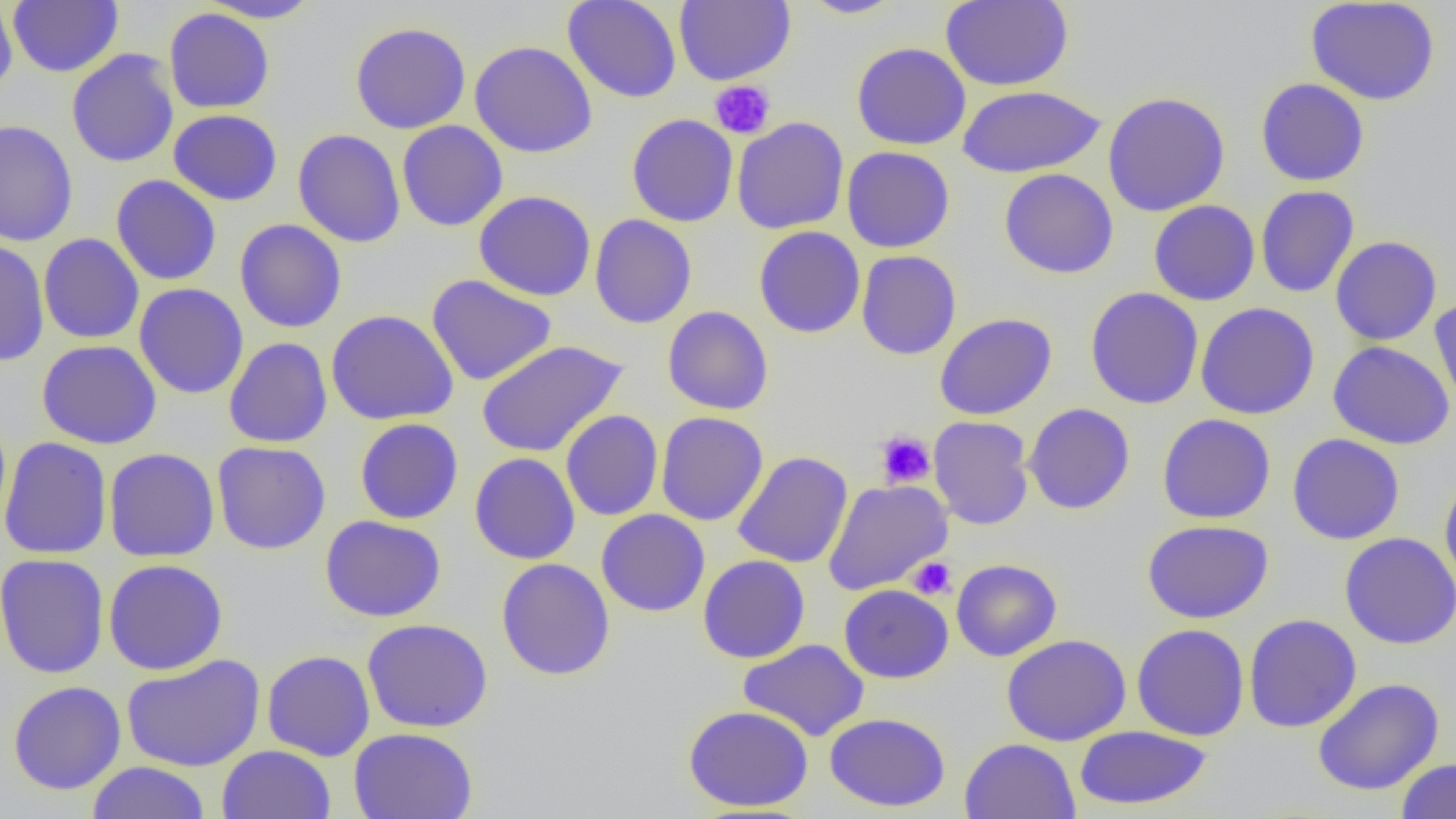 Approximate bounding boxes as (x1,y1)-(x2,y2) corner pairs in pixels. Platelet locations: (709,80)-(775,139), (875,430)-(935,489), (908,557)-(956,599). Uninfected red blood cell locations: (0,0)-(18,97), (197,0)-(325,23), (562,0)-(682,103), (674,0)-(795,86), (797,0)-(908,19), (940,0)-(1073,91), (8,1)-(123,77), (1304,1)-(1440,106), (164,8)-(274,113), (350,21)-(472,134), (470,40)-(598,158), (851,42)-(971,150), (66,49)-(179,168), (1255,77)-(1369,186), (958,85)-(1106,178), (1102,91)-(1230,216), (168,109)-(282,206), (626,113)-(739,226), (732,116)-(849,234), (0,120)-(79,247), (397,120)-(508,231), (293,128)-(406,248), (841,146)-(956,253), (999,168)-(1118,279), (111,174)-(222,285), (1255,185)-(1360,298), (473,190)-(596,301), (1148,200)-(1260,306), (589,214)-(697,329), (234,219)-(347,333), (754,226)-(865,338), (38,233)-(144,344), (1331,236)-(1442,345), (0,237)-(49,366), (856,250)-(962,360), (426,274)-(557,386), (134,283)-(249,399), (1085,287)-(1203,409), (1429,298)-(1456,416), (1195,302)-(1320,420), (662,306)-(774,415), (326,308)-(459,426), (934,313)-(1057,420), (224,337)-(333,448), (36,339)-(162,449), (476,339)-(629,458), (1327,340)-(1454,450), (1023,403)-(1135,515), (561,410)-(663,521), (655,411)-(769,526), (1157,413)-(1276,524), (929,416)-(1035,530), (354,418)-(464,524), (1287,433)-(1405,545), (0,437)-(112,559), (212,441)-(331,554), (103,447)-(220,562), (733,451)-(853,568), (469,452)-(580,565), (1439,472)-(1456,595), (823,479)-(952,595), (596,509)-(710,616), (320,514)-(446,622), (1142,520)-(1274,623), (1339,532)-(1456,650), (0,553)-(109,678), (698,555)-(810,663), (103,558)-(228,675), (496,558)-(615,680), (951,559)-(1062,661), (838,583)-(954,683), (1243,613)-(1362,733), (362,617)-(493,733), (1132,623)-(1250,741), (1001,634)-(1132,746), (738,639)-(869,741), (261,650)-(375,761), (121,653)-(265,772), (1313,677)-(1444,795), (8,680)-(126,795), (683,705)-(814,812), (824,712)-(951,811), (1074,724)-(1212,812), (348,727)-(478,819), (960,738)-(1080,818), (217,745)-(336,819), (1396,757)-(1456,818), (87,761)-(212,819). Slide-level diagnosis: no evidence of blood parasites. Image is 1456×819 pixels. Thin blood film. 1000x magnification. One field of a larger specimen. Optical microscopy.